Give the position of every leukocyte visible.
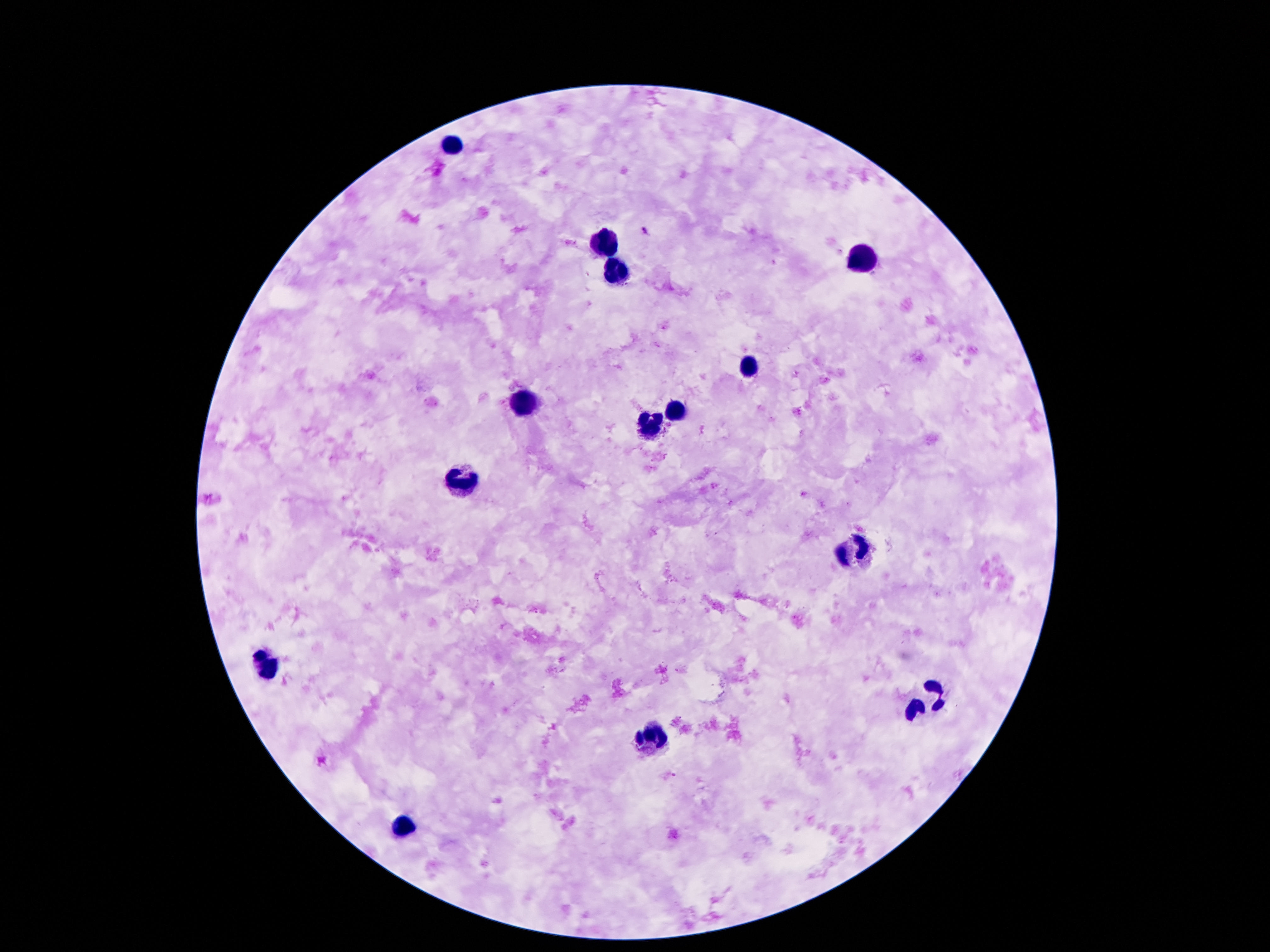

Approximate object centers, in pixels from the top-left corner.
Leukocytes: (x=454, y=144), (x=606, y=242), (x=863, y=264), (x=615, y=274), (x=749, y=368), (x=527, y=403), (x=672, y=415), (x=649, y=426), (x=463, y=480), (x=854, y=548), (x=266, y=663), (x=924, y=703), (x=649, y=738), (x=400, y=828).

Summary:
  - Magnification: 100x
  - Patient malaria status: negative
  - Image size: 1270×952 pixels
  - Stain: Giemsa
  - Preparation: thick blood smear
  - Field of view: single
  - Capture: smartphone camera through the microscope eyepiece